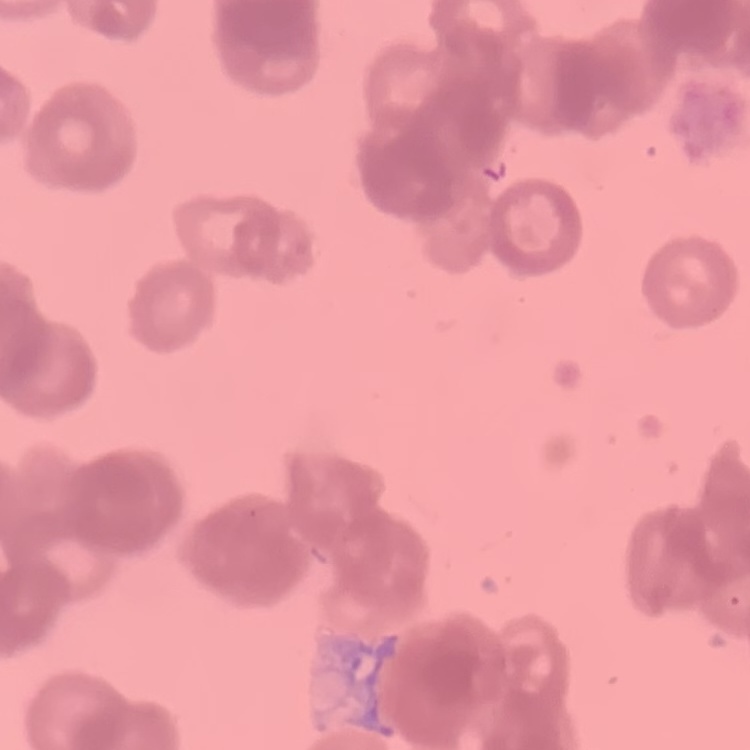
The red blood cells exhibit rouleaux formation. Field's or Giemsa stain. Square crop of a larger photomicrograph. Thin blood film.